Assess this cell for malaria.
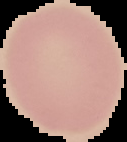
It is uninfected.

Segmented cell region on a black background. From a thin blood smear. Image is 127×142 pixels.